Classify this cell by malaria status.
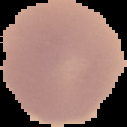
Uninfected.

Summary:
  - Preparation: thin blood smear
  - Image size: 127×127 pixels
  - Image type: segmented cell region on a black background